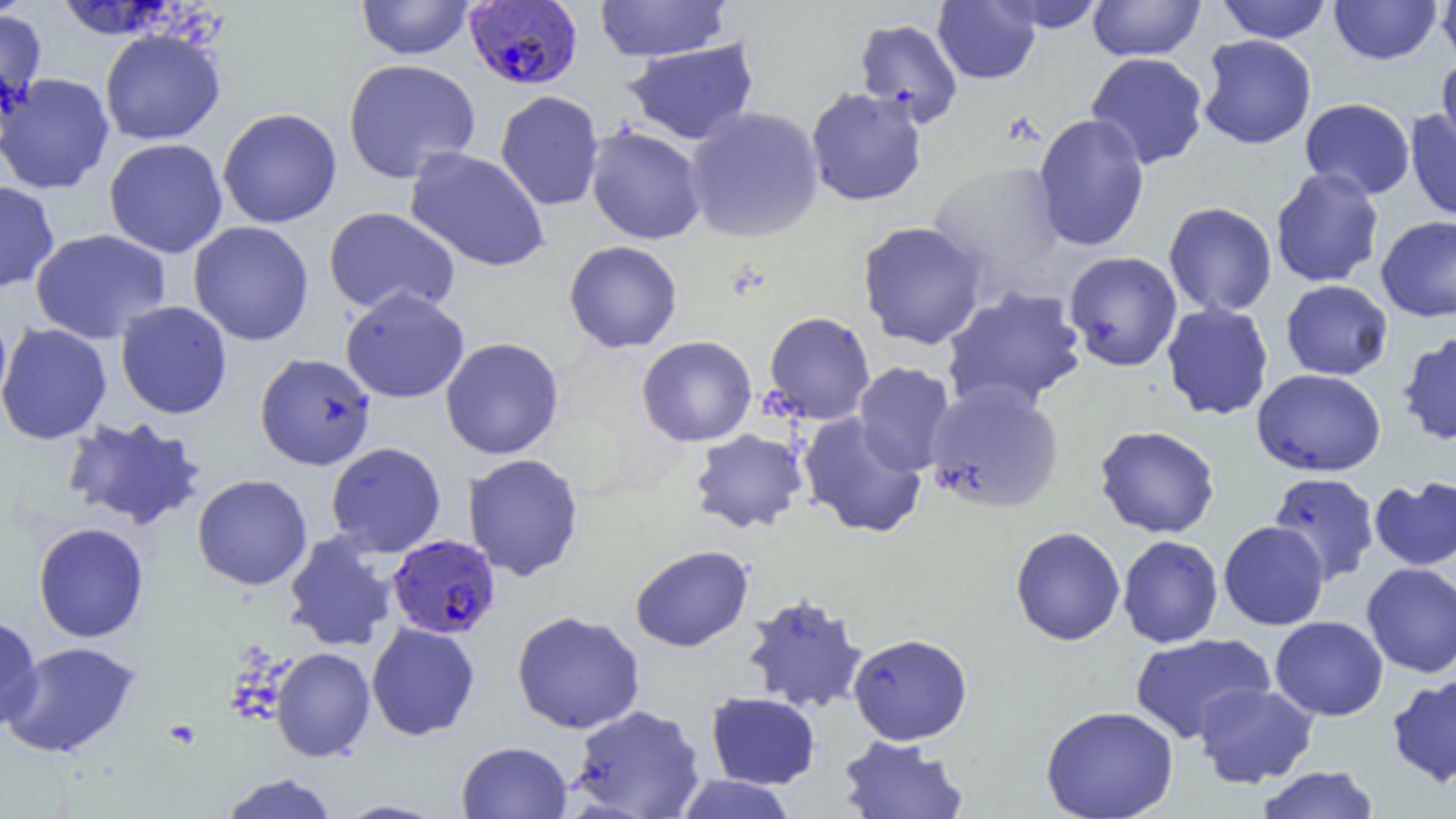

{
  "slide_level_diagnosis": "Plasmodium falciparum",
  "magnification": "1000x",
  "platelet_locations": "approximate bounding boxes as named x1/y1/x2/y2 corners in pixels: (x1=164, y1=719, x2=201, y2=749)",
  "uninfected_red_blood_cell_locations": "approximate bounding boxes as named x1/y1/x2/y2 corners in pixels: (x1=356, y1=0, x2=475, y2=60), (x1=594, y1=0, x2=731, y2=62), (x1=933, y1=0, x2=1041, y2=84), (x1=993, y1=0, x2=1108, y2=32), (x1=1087, y1=0, x2=1206, y2=61), (x1=1329, y1=0, x2=1442, y2=64), (x1=1436, y1=0, x2=1456, y2=69), (x1=54, y1=1, x2=175, y2=40), (x1=1216, y1=1, x2=1332, y2=42), (x1=0, y1=7, x2=48, y2=123), (x1=853, y1=18, x2=963, y2=127), (x1=99, y1=28, x2=226, y2=145), (x1=1198, y1=34, x2=1316, y2=149), (x1=623, y1=38, x2=759, y2=146), (x1=1085, y1=52, x2=1209, y2=169), (x1=1437, y1=56, x2=1456, y2=161), (x1=342, y1=58, x2=481, y2=183), (x1=0, y1=72, x2=114, y2=194), (x1=805, y1=86, x2=928, y2=207), (x1=495, y1=90, x2=604, y2=211), (x1=1300, y1=97, x2=1416, y2=200), (x1=684, y1=106, x2=824, y2=243), (x1=217, y1=108, x2=342, y2=228), (x1=1405, y1=108, x2=1456, y2=222), (x1=1032, y1=113, x2=1150, y2=252), (x1=585, y1=126, x2=706, y2=244), (x1=104, y1=138, x2=228, y2=258), (x1=405, y1=147, x2=550, y2=272), (x1=927, y1=160, x2=1067, y2=287), (x1=1270, y1=167, x2=1384, y2=287), (x1=0, y1=181, x2=60, y2=293), (x1=1163, y1=201, x2=1277, y2=317), (x1=323, y1=206, x2=461, y2=317), (x1=1376, y1=215, x2=1456, y2=322), (x1=856, y1=220, x2=989, y2=350), (x1=188, y1=221, x2=314, y2=346), (x1=30, y1=228, x2=171, y2=345), (x1=563, y1=240, x2=683, y2=353), (x1=1063, y1=250, x2=1182, y2=372), (x1=1281, y1=280, x2=1393, y2=380), (x1=940, y1=285, x2=1088, y2=413), (x1=340, y1=287, x2=469, y2=404), (x1=115, y1=301, x2=232, y2=419), (x1=1161, y1=301, x2=1273, y2=421), (x1=0, y1=309, x2=13, y2=419), (x1=764, y1=311, x2=876, y2=424), (x1=0, y1=323, x2=112, y2=445), (x1=1396, y1=330, x2=1456, y2=447), (x1=636, y1=335, x2=757, y2=447), (x1=440, y1=337, x2=564, y2=460), (x1=254, y1=353, x2=376, y2=470), (x1=853, y1=362, x2=957, y2=475), (x1=1252, y1=368, x2=1386, y2=476), (x1=924, y1=382, x2=1065, y2=513), (x1=798, y1=412, x2=927, y2=539), (x1=61, y1=416, x2=208, y2=532), (x1=1094, y1=425, x2=1220, y2=538), (x1=689, y1=428, x2=809, y2=534), (x1=326, y1=442, x2=446, y2=557), (x1=462, y1=453, x2=584, y2=582), (x1=1269, y1=472, x2=1380, y2=584), (x1=192, y1=474, x2=312, y2=590), (x1=1369, y1=475, x2=1456, y2=571), (x1=1218, y1=521, x2=1329, y2=630), (x1=33, y1=522, x2=149, y2=643), (x1=1010, y1=526, x2=1125, y2=645), (x1=283, y1=532, x2=398, y2=652), (x1=1117, y1=535, x2=1223, y2=648), (x1=630, y1=545, x2=753, y2=652), (x1=1361, y1=563, x2=1456, y2=678), (x1=742, y1=592, x2=869, y2=714), (x1=511, y1=610, x2=645, y2=734), (x1=0, y1=612, x2=43, y2=731), (x1=1270, y1=616, x2=1388, y2=721), (x1=366, y1=622, x2=480, y2=741), (x1=1130, y1=632, x2=1275, y2=743), (x1=848, y1=633, x2=973, y2=745), (x1=2, y1=641, x2=141, y2=758), (x1=271, y1=647, x2=375, y2=762), (x1=1386, y1=674, x2=1456, y2=789), (x1=1193, y1=682, x2=1319, y2=788), (x1=706, y1=691, x2=821, y2=789), (x1=569, y1=704, x2=706, y2=818), (x1=1041, y1=705, x2=1179, y2=818), (x1=837, y1=735, x2=969, y2=818), (x1=456, y1=740, x2=573, y2=819), (x1=1255, y1=765, x2=1380, y2=819), (x1=219, y1=773, x2=339, y2=819), (x1=673, y1=774, x2=799, y2=819), (x1=333, y1=800, x2=449, y2=819)",
  "field_of_view": "one of a larger specimen",
  "modality": "optical microscopy",
  "preparation": "thin blood smear",
  "plasmodium_falciparum_infected_red_blood_cell_locations": "approximate bounding boxes as named x1/y1/x2/y2 corners in pixels: (x1=464, y1=1, x2=583, y2=91), (x1=387, y1=534, x2=501, y2=640)",
  "image_size": "1456×819 pixels"
}